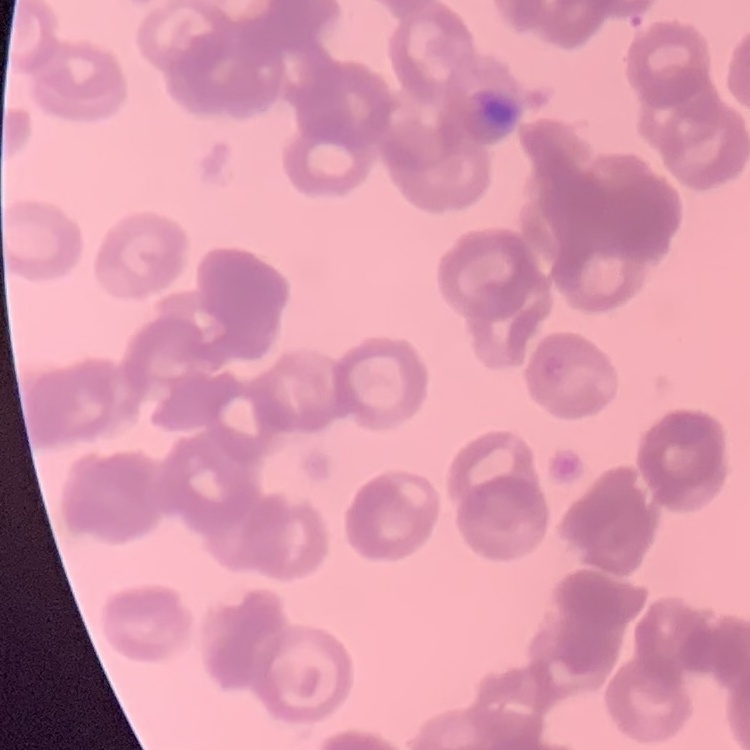

Summary:
  - Erythrocyte morphology: rouleaux formation
  - Preparation: thin peripheral smear
  - Image type: square crop of a larger photomicrograph
  - Stain: Field's or Giemsa